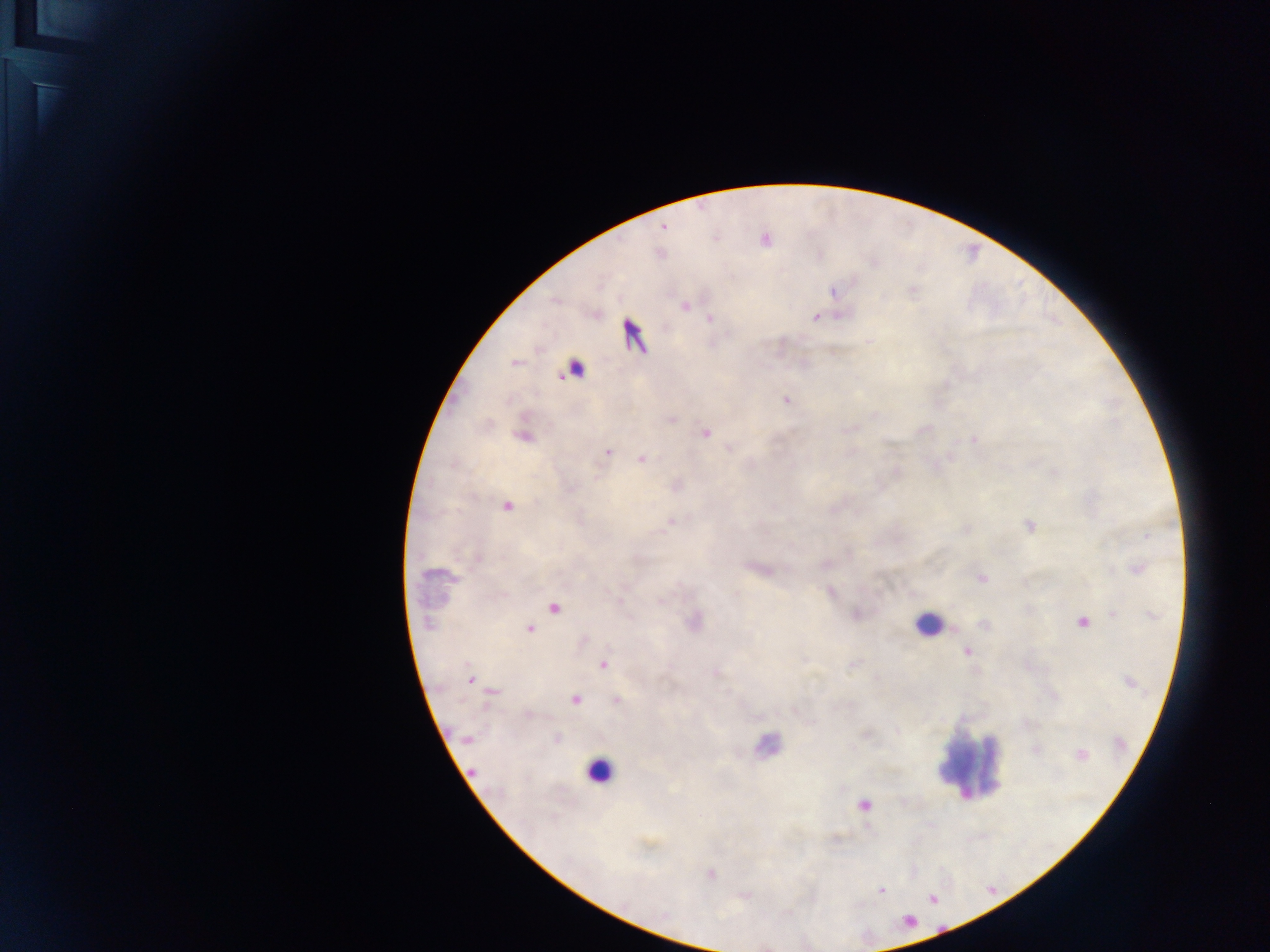 Approximate centers as [x, y] in pixels. Malaria parasite locations: [664, 228], [685, 307], [815, 317], [710, 318], [514, 362], [786, 400], [672, 420], [705, 433], [524, 437], [973, 440], [608, 452], [642, 459], [598, 478], [507, 507], [671, 521], [1029, 526], [1148, 535], [1138, 568], [981, 578], [554, 608], [1114, 614], [1082, 622], [428, 623], [529, 628], [966, 651], [602, 664], [470, 680], [493, 692], [575, 700], [617, 700], [528, 714], [557, 738], [466, 739], [1081, 754], [473, 771], [864, 805], [711, 873], [881, 891]. Leukocyte locations: [575, 366], [927, 624], [968, 764], [599, 771]. Image is 1270×952 pixels. Single field of view. Collected in Ghana. Photographed through a microscope with a mobile-phone camera. Thick blood film.